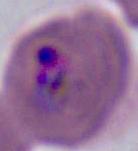
Summary:
  - Identification: Plasmodium
  - Magnification: 400x or 1000x
  - Modality: micrograph